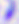

Summary:
  - Magnification: 400x
  - Modality: photomicrograph
  - Identification: Toxoplasma gondii